Classify this cell by malaria status.
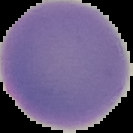
It is uninfected.

From a thin blood film. Image is 133×133 pixels. Cell region segmented out of the field of view; the surrounding area is masked to black.